Assess this cell for malaria.
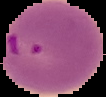

It is parasitized.

Summary:
  - Preparation: thin blood smear
  - Image type: cell region segmented out of the field of view; surrounding area masked to black
  - Image size: 106×97 pixels